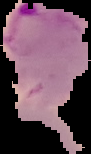

Image is 91×154 pixels. From a thin blood film. The area outside the segmented cell region is set to black. Malaria status: parasitized.